Locate every blood parasite and identify its species.
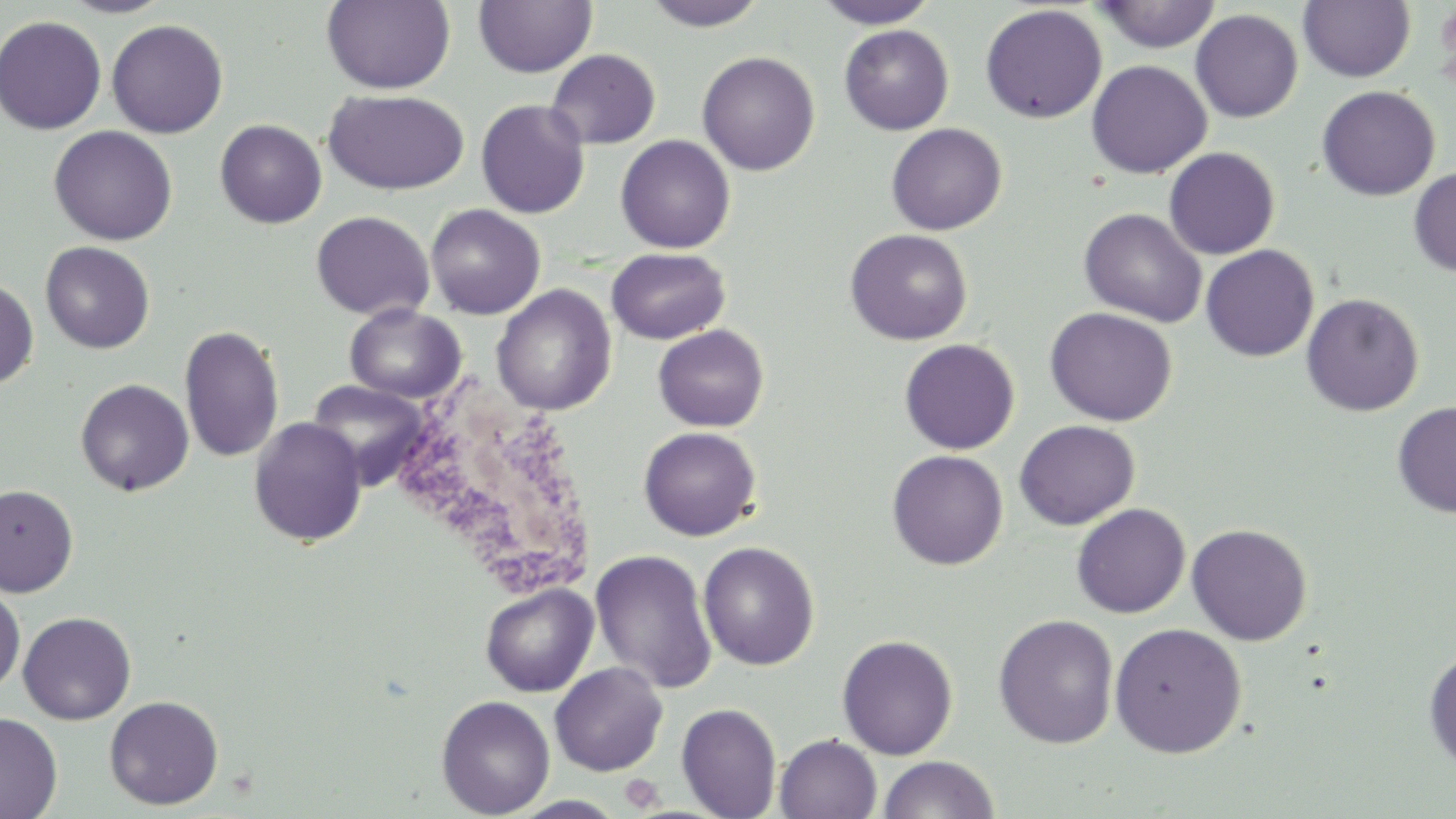
No blood parasites seen.

slide-level diagnosis = no evidence of blood parasites
uninfected red blood cell locations = approximate bounding boxes as [x1, y1, x2, y2] in pixels: [57, 0, 175, 19], [321, 0, 455, 94], [644, 0, 767, 31], [813, 0, 940, 28], [1298, 0, 1415, 82], [473, 1, 597, 78], [1093, 1, 1222, 53], [980, 5, 1107, 124], [1190, 9, 1303, 122], [0, 15, 106, 135], [106, 19, 228, 138], [839, 24, 954, 135], [546, 48, 660, 149], [697, 51, 820, 176], [1086, 60, 1211, 178], [1316, 85, 1440, 200], [322, 88, 469, 195], [475, 99, 590, 219], [214, 119, 327, 228], [886, 123, 1007, 235], [49, 125, 178, 245], [615, 134, 736, 253], [1164, 147, 1280, 259], [1409, 166, 1456, 277], [425, 204, 545, 320], [1078, 207, 1207, 327], [311, 210, 434, 320], [845, 228, 972, 345], [40, 241, 155, 353], [1201, 244, 1319, 361], [606, 247, 730, 345], [0, 277, 38, 390], [492, 284, 617, 415], [1301, 293, 1424, 416], [344, 304, 466, 404], [1044, 307, 1177, 426], [178, 324, 285, 463], [653, 324, 769, 431], [899, 338, 1020, 454], [75, 378, 194, 496], [307, 380, 430, 489], [1392, 401, 1456, 518], [248, 416, 368, 547], [1014, 419, 1139, 530], [638, 426, 761, 540], [887, 449, 1008, 570], [0, 485, 78, 597], [1071, 503, 1190, 618], [1069, 514, 1309, 626], [1187, 523, 1312, 645], [698, 541, 820, 670], [589, 549, 718, 693], [479, 583, 599, 697], [0, 585, 25, 694], [18, 611, 136, 724], [992, 613, 1119, 748], [1109, 622, 1247, 758], [836, 634, 959, 760], [1423, 649, 1456, 773], [550, 663, 668, 776], [104, 695, 224, 810], [436, 695, 555, 818], [677, 702, 782, 819], [0, 712, 62, 818], [775, 734, 882, 819], [877, 755, 999, 818], [508, 795, 629, 818]
preparation = thin blood film
image size = 1456×819 pixels
platelet locations = approximate bounding boxes as [x1, y1, x2, y2] in pixels: [620, 774, 664, 812]
white blood cell locations = approximate bounding boxes as [x1, y1, x2, y2] in pixels: [387, 375, 598, 604]
field of view = single
stain = May-Grünwald-Giemsa
magnification = 1000x
modality = light microscopy